Assess this cell for malaria.
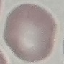

It is uninfected.

Automatically extracted cell patch, resized to 64 × 64 pixels. Giemsa-stained preparation. Photographed with a smartphone camera at the microscope eyepiece. Thin blood smear.